Report the malaria status of this cell.
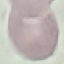

It is uninfected.

Summary:
  - Image type: cell patch, automatically extracted from a larger field of view and resized to 64 × 64 pixels
  - Preparation: thin blood smear
  - Capture: smartphone camera at the microscope eyepiece
  - Stain: Giemsa